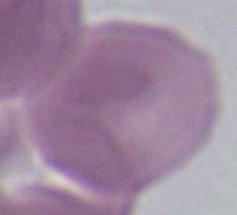
identification = erythrocyte
magnification = 1000x
modality = micrograph